Comment on the morphology of the red blood cells.
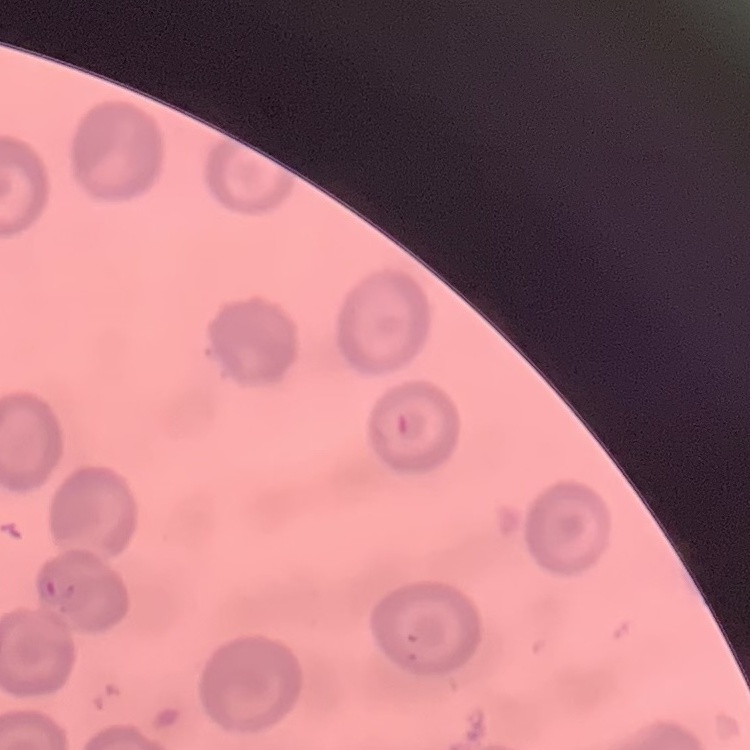

They show no rouleaux formation.

image type = square crop of a larger photomicrograph
stain = Field's or Giemsa
preparation = thin blood film